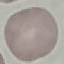

result = no malaria parasites seen
image type = cell patch, automatically extracted from a larger field of view and resized to 64 × 64 pixels
capture = smartphone camera at the microscope eyepiece
stain = Giemsa
preparation = thin blood smear